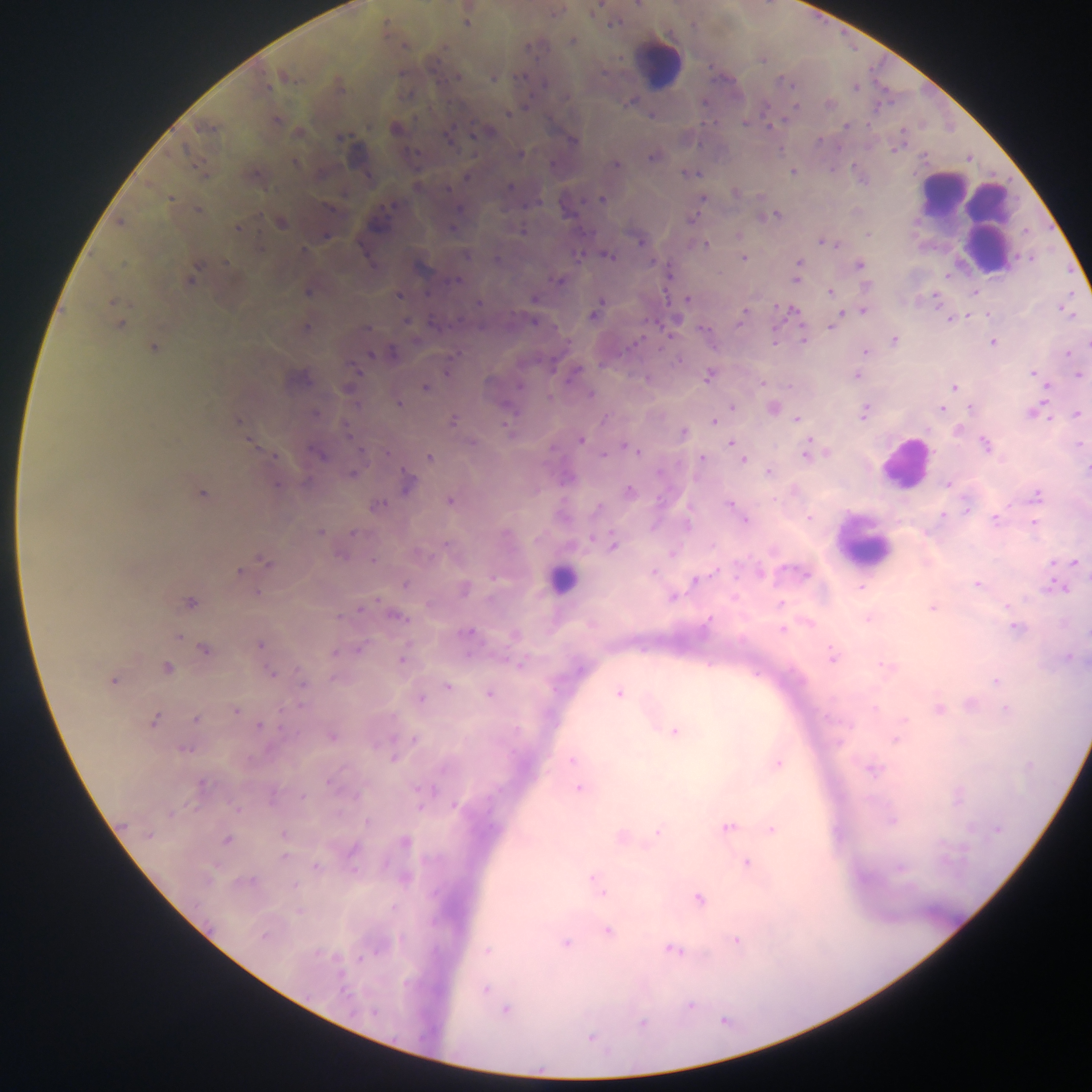

Approximate centers as {x, y} in pixels. Malaria parasite locations: {638, 4}, {556, 11}, {466, 23}, {614, 23}, {572, 41}, {531, 47}, {284, 76}, {457, 77}, {494, 78}, {544, 83}, {267, 87}, {829, 105}, {509, 113}, {277, 121}, {744, 122}, {846, 126}, {206, 128}, {396, 129}, {485, 131}, {340, 137}, {449, 139}, {573, 141}, {520, 154}, {651, 157}, {295, 164}, {616, 164}, {792, 171}, {689, 173}, {466, 177}, {510, 188}, {735, 192}, {170, 198}, {602, 199}, {702, 199}, {392, 206}, {330, 209}, {460, 209}, {198, 210}, {771, 217}, {691, 219}, {120, 223}, {281, 223}, {238, 228}, {453, 228}, {868, 234}, {326, 236}, {639, 242}, {827, 243}, {705, 245}, {304, 251}, {466, 254}, {607, 255}, {579, 256}, {743, 258}, {496, 259}, {227, 263}, {799, 263}, {860, 266}, {195, 271}, {797, 271}, {796, 278}, {190, 280}, {456, 280}, {559, 280}, {307, 292}, {830, 292}, {399, 296}, {535, 299}, {687, 299}, {112, 302}, {478, 302}, {596, 308}, {863, 310}, {790, 311}, {593, 314}, {743, 316}, {951, 319}, {406, 321}, {534, 322}, {120, 324}, {832, 325}, {306, 328}, {366, 328}, {704, 329}, {774, 338}, {893, 340}, {803, 341}, {993, 342}, {154, 347}, {865, 352}, {1068, 353}, {371, 355}, {447, 372}, {574, 373}, {1033, 374}, {708, 376}, {856, 376}, {1078, 376}, {761, 382}, {520, 385}, {426, 388}, {954, 388}, {349, 390}, {590, 395}, {399, 403}, {732, 407}, {772, 408}, {971, 408}, {941, 409}, {863, 412}, {1034, 412}, {1077, 414}, {797, 419}, {454, 421}, {713, 421}, {238, 422}, {506, 425}, {958, 429}, {348, 432}, {684, 432}, {580, 440}, {472, 442}, {731, 443}, {1080, 444}, {985, 445}, {629, 448}, {634, 451}, {387, 453}, {317, 454}, {807, 454}, {273, 455}, {604, 456}, {429, 457}, {701, 459}, {743, 459}, {1087, 470}, {768, 472}, {352, 475}, {408, 483}, {276, 485}, {947, 485}, {629, 491}, {202, 493}, {1036, 496}, {450, 501}, {729, 504}, {377, 506}, {598, 508}, {967, 509}, {944, 515}, {809, 518}, {995, 519}, {744, 520}, {687, 524}, {1034, 524}, {320, 532}, {353, 533}, {506, 534}, {591, 539}, {614, 546}, {673, 553}, {341, 555}, {373, 561}, {265, 563}, {1075, 563}, {246, 567}, {789, 570}, {239, 572}, {760, 572}, {652, 573}, {804, 574}, {696, 580}, {405, 585}, {977, 585}, {1057, 587}, {861, 588}, {465, 591}, {673, 597}, {190, 602}, {781, 604}, {1007, 607}, {932, 608}, {360, 609}, {399, 618}, {868, 619}, {707, 621}, {1016, 627}, {782, 630}, {467, 633}, {1087, 633}, {178, 636}, {260, 644}, {361, 648}, {204, 650}, {335, 653}, {832, 657}, {1069, 658}, {402, 660}, {520, 664}, {887, 666}, {166, 668}, {271, 674}, {995, 681}, {113, 682}, {302, 682}, {448, 687}, {489, 694}, {619, 694}, {422, 699}, {938, 709}, {1006, 709}, {236, 710}, {196, 719}, {154, 721}, {261, 726}, {674, 731}, {332, 737}, {896, 739}, {415, 740}, {184, 749}, {393, 758}, {571, 760}, {778, 763}, {873, 770}, {330, 784}, {201, 785}, {578, 789}, {420, 790}, {303, 797}, {455, 806}, {236, 808}, {170, 813}, {892, 821}, {367, 822}, {728, 827}, {772, 829}, {997, 829}, {658, 832}, {148, 835}, {227, 839}, {405, 843}, {353, 850}, {284, 856}, {747, 862}, {316, 866}, {900, 868}, {405, 878}, {595, 880}, {245, 882}, {599, 890}, {699, 899}, {608, 930}, {264, 936}, {737, 940}, {565, 942}, {673, 949}, {488, 950}, {485, 990}, {690, 1006}, {506, 1010}, {373, 1013}, {643, 1023}, {590, 1037}. Leukocyte locations: {658, 62}, {942, 192}, {971, 215}, {903, 463}, {866, 540}, {561, 580}. Image is 1092×1092 pixels. Thick blood film. Collected in Ghana. Mobile-phone photograph taken through the microscope. Single field of view.